Classify this cell by malaria status.
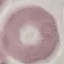

Uninfected.

Giemsa stain. Thin blood film. Photographed with a smartphone camera at the microscope eyepiece. Automatically extracted cell patch, resized to 64 × 64 pixels.